Give the position of every leukocyte visible.
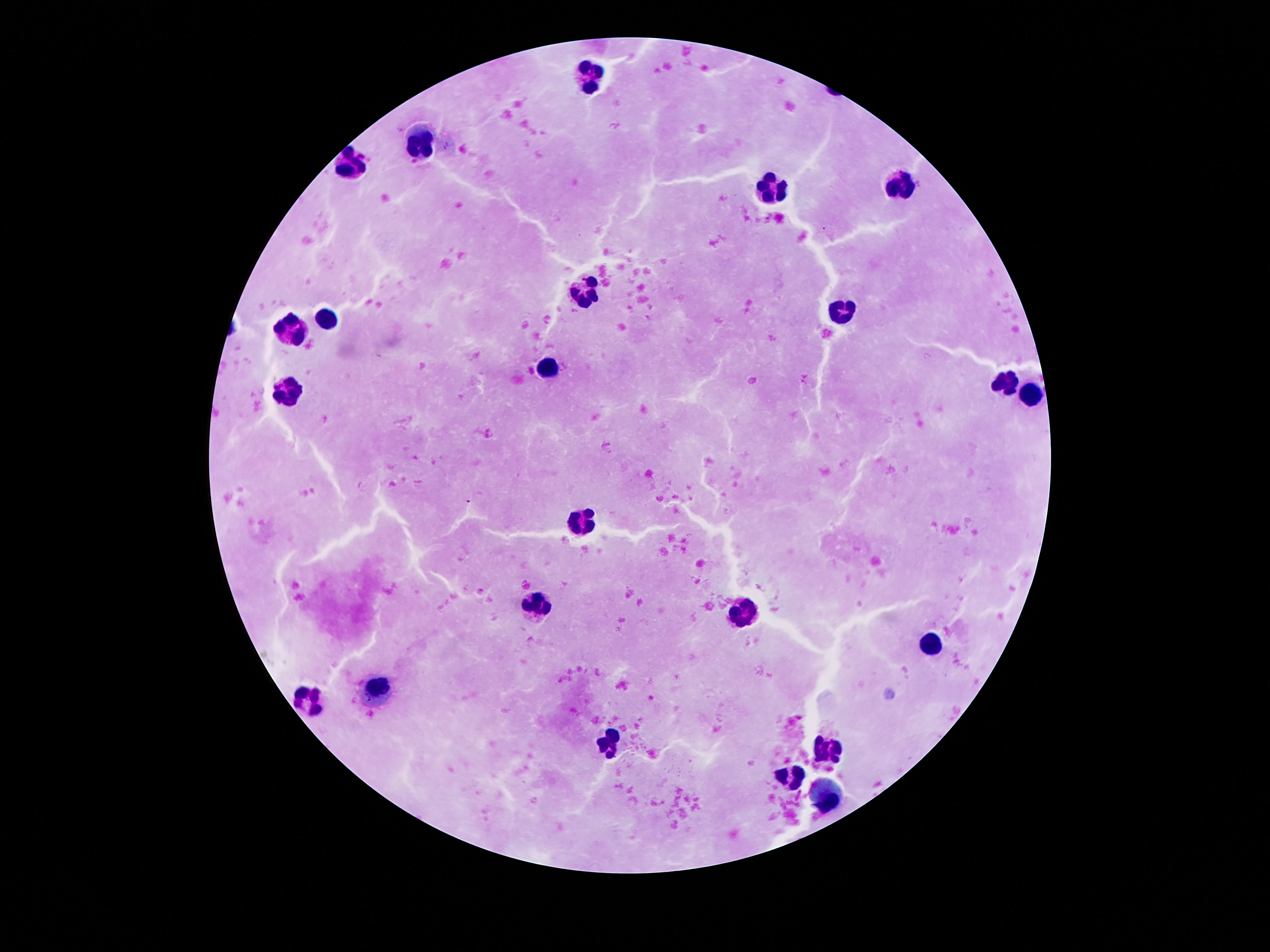
Approximate centers as {x, y} in pixels.
Leukocytes: {591, 76}, {422, 142}, {356, 161}, {902, 182}, {769, 186}, {582, 290}, {843, 310}, {328, 317}, {292, 328}, {549, 367}, {1007, 384}, {290, 390}, {1032, 397}, {582, 522}, {539, 604}, {742, 615}, {928, 644}, {378, 688}, {312, 699}, {614, 744}, {828, 747}, {793, 780}, {830, 790}.

{
  "image_size": "1270×952 pixels",
  "capture": "smartphone camera through the microscope eyepiece",
  "magnification": "100x",
  "preparation": "thick blood film",
  "stain": "Giemsa",
  "field_of_view": "single",
  "patient_malaria_status": "uninfected"
}